Describe the morphology of the red blood cells.
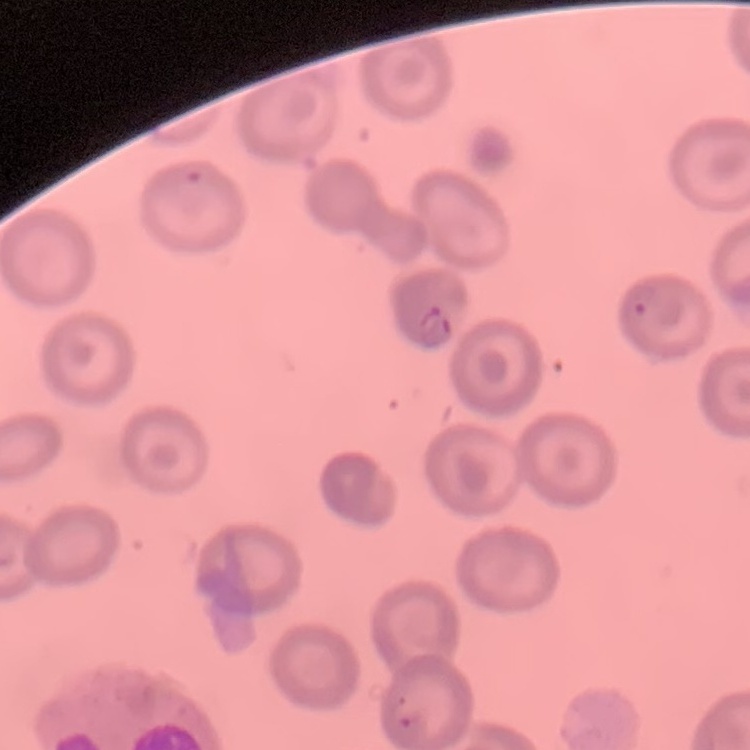

They show no rouleaux formation.

Field's or Giemsa stain. One tile cut from a larger photomicrograph. Thin peripheral smear.